Identify the cell.
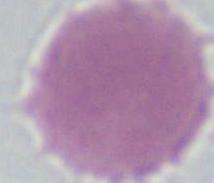
An erythrocyte.

1000x magnification. Micrograph.